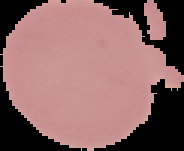
From a thin blood film. Malaria status: uninfected. Segmented cell region on a black background. Image is 184×151 pixels.